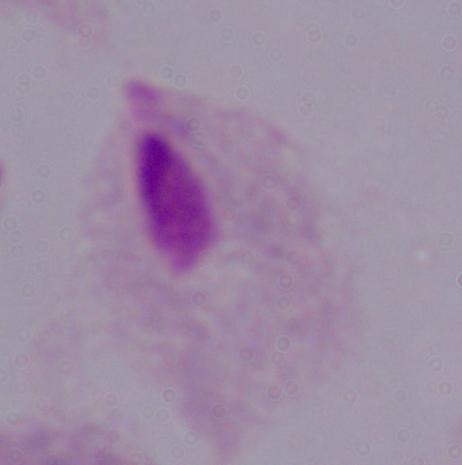
identification = trichomonad
magnification = 1000x
modality = photomicrograph